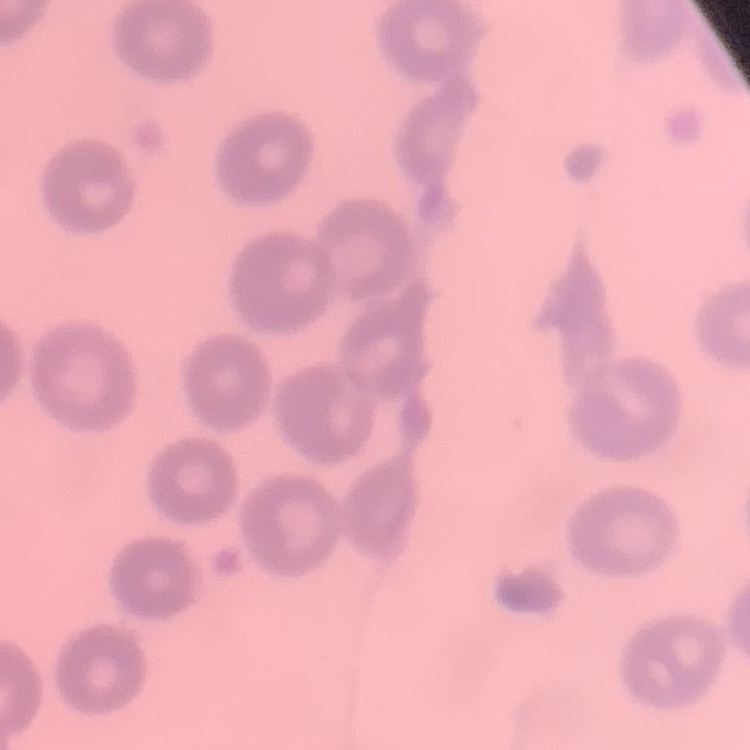
{
  "erythrocyte_morphology": "no rouleaux formation",
  "stain": "Field's or Giemsa",
  "preparation": "thin blood smear",
  "image_type": "one tile cut from a larger photomicrograph"
}